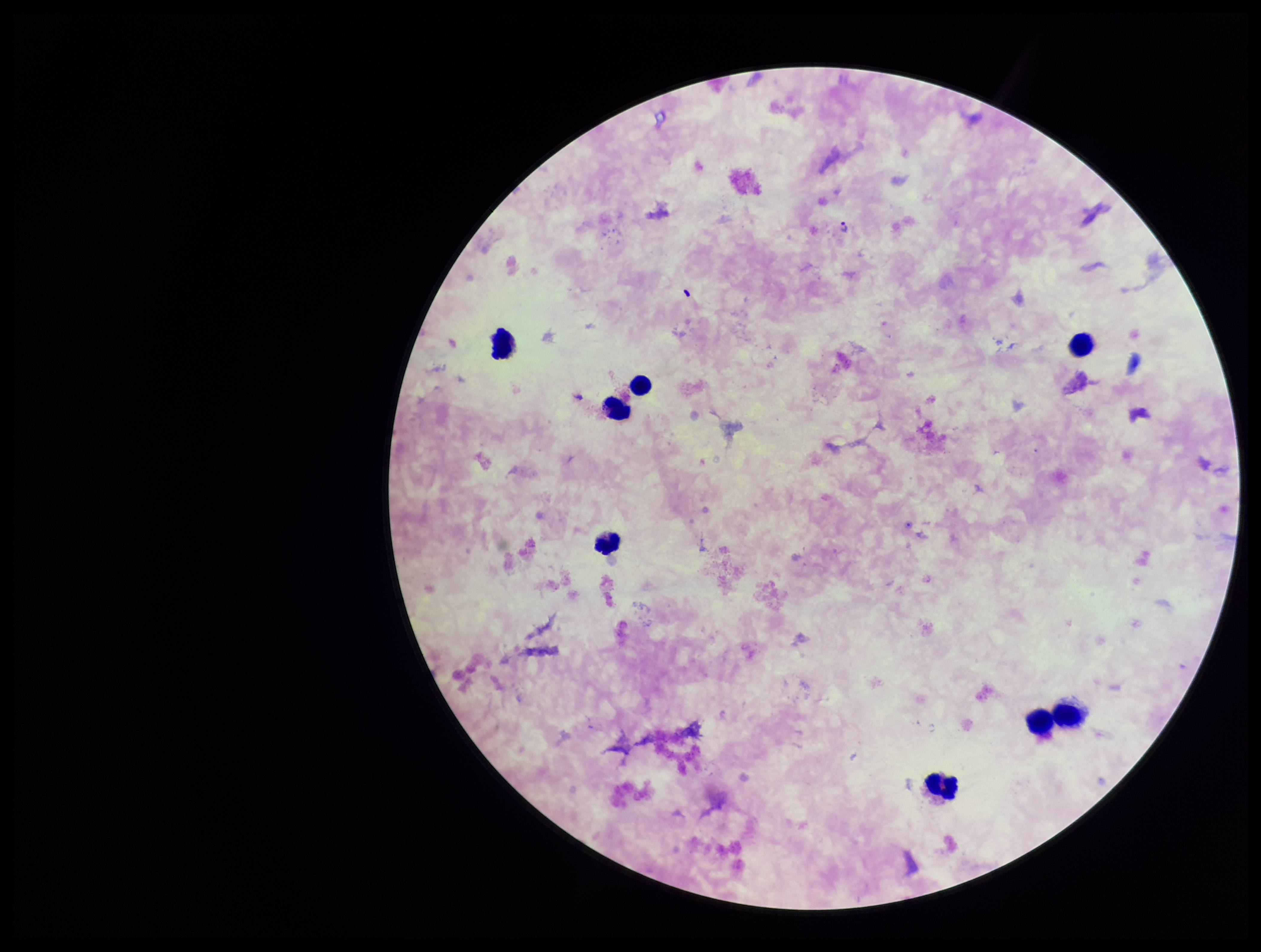

image size = 1261×952 pixels
stain = Giemsa
leukocyte count = 8
capture = smartphone photograph through the microscope eyepiece
Plasmodium parasites = none seen
preparation = thick smear
parasite count = 0
patient malaria status = infected
field of view = one from this slide
species reported for this patient = Plasmodium falciparum